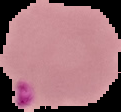
Summary:
  - Image type: cell region segmented out of the field of view; surrounding area masked to black
  - Result: Plasmodium parasites detected
  - Image size: 121×112 pixels
  - Preparation: thin blood smear